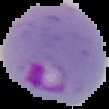
{
  "image_size": "109×109 pixels",
  "image_type": "cell region segmented out of the field of view; surrounding area masked to black",
  "result": "Plasmodium parasites detected",
  "preparation": "thin blood film"
}